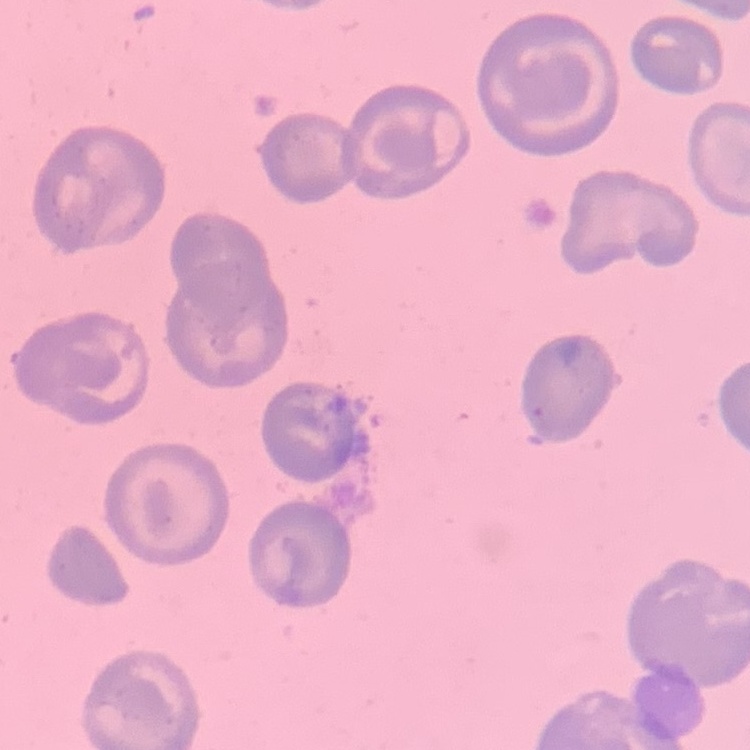
The red blood cells exhibit no rouleaux formation. Stained with either Field's or Giemsa. Thin blood smear. One tile cut from a larger photomicrograph.